Identify the parasite.
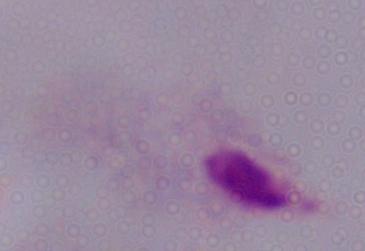
This is a trichomonad.

1000x magnification. Micrograph.